State the blood parasite species.
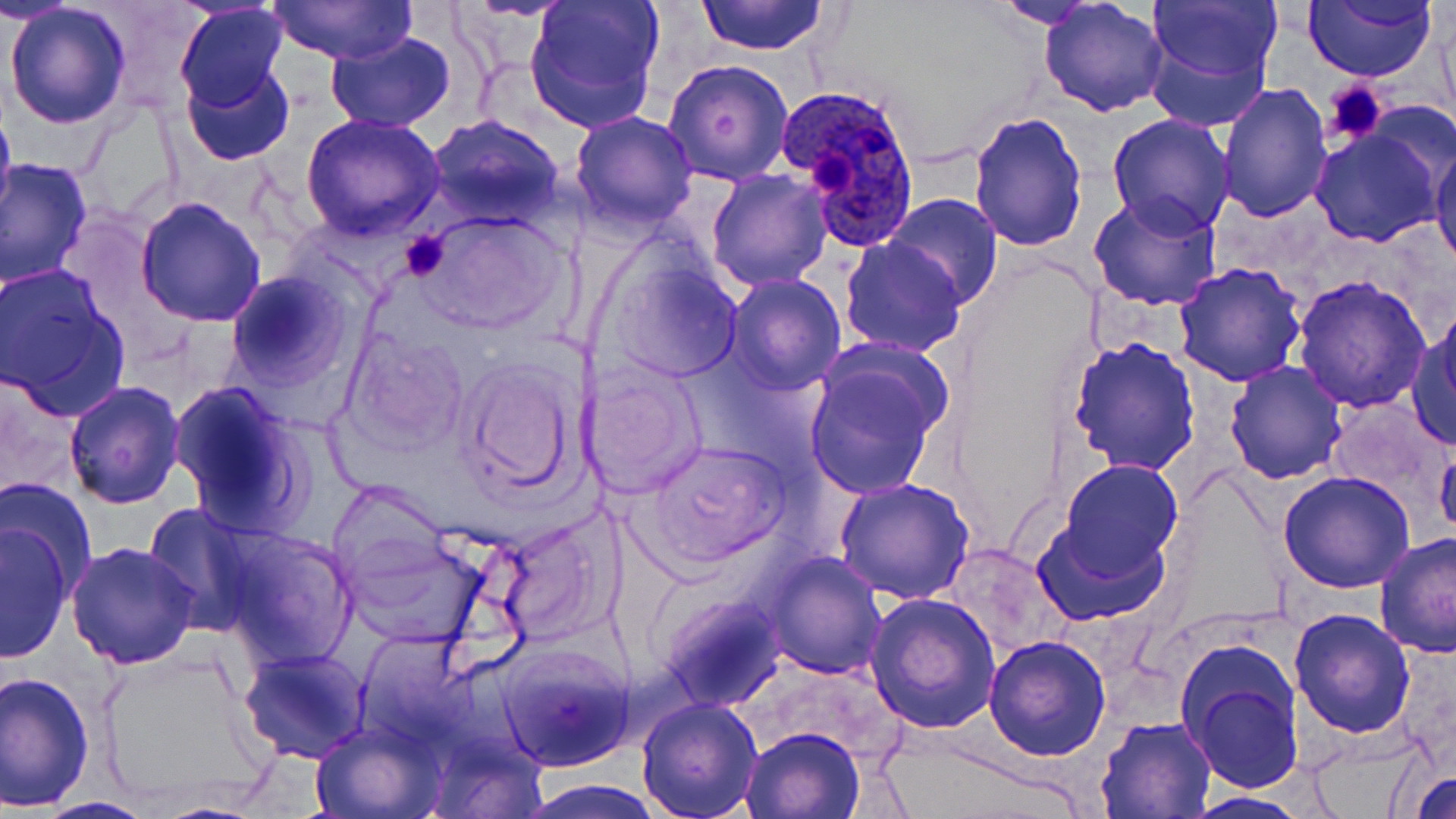
Plasmodium ovale.

Summary:
  - Coordinate format: approximate bounding boxes as (x1, y1, x2, y2) in pixels
  - Platelet locations: (1324, 79, 1387, 145), (400, 229, 453, 281)
  - Plasmodium ovale-infected red blood cell locations: (778, 84, 925, 252)
  - Uninfected red blood cell locations: (3, 0, 78, 26), (463, 0, 577, 21), (522, 0, 666, 132), (696, 0, 829, 55), (990, 0, 1109, 29), (1040, 0, 1168, 117), (1143, 0, 1280, 98), (1303, 0, 1438, 82), (269, 1, 416, 64), (5, 3, 132, 129), (174, 5, 289, 113), (324, 31, 456, 130), (663, 59, 793, 186), (182, 62, 295, 167), (1216, 82, 1333, 224), (0, 96, 16, 235), (968, 110, 1089, 252), (569, 111, 700, 232), (1106, 114, 1235, 238), (300, 115, 447, 242), (427, 116, 564, 227), (1308, 126, 1443, 247), (1430, 136, 1456, 271), (1, 157, 94, 290), (706, 170, 832, 292), (1090, 191, 1225, 313), (882, 195, 1005, 308), (135, 197, 266, 327), (414, 212, 568, 336), (839, 236, 967, 356), (597, 247, 745, 385), (1173, 262, 1308, 386), (0, 263, 130, 416), (226, 270, 351, 391), (723, 274, 846, 395), (1291, 274, 1431, 413), (1409, 320, 1456, 449), (345, 330, 471, 454), (1068, 335, 1200, 474), (804, 356, 945, 500), (459, 357, 585, 499), (1224, 360, 1348, 484), (580, 362, 707, 498), (63, 381, 185, 509), (168, 381, 313, 536), (1329, 398, 1453, 513), (642, 439, 792, 565), (1435, 439, 1456, 542), (1057, 459, 1182, 576), (1278, 471, 1417, 593), (1, 477, 98, 597), (834, 478, 975, 605), (331, 480, 448, 587), (137, 502, 265, 632), (1032, 516, 1171, 625), (491, 517, 614, 644), (0, 523, 74, 661), (217, 530, 359, 669), (1374, 531, 1455, 658), (338, 532, 493, 652), (66, 540, 200, 670), (943, 544, 1060, 657), (765, 553, 886, 679), (864, 591, 1001, 734), (660, 596, 781, 710), (1288, 608, 1417, 738), (984, 633, 1110, 760), (498, 642, 633, 772), (237, 648, 371, 765), (101, 651, 269, 810), (1179, 651, 1305, 793), (1, 669, 96, 810), (636, 697, 763, 819), (1097, 716, 1216, 817), (310, 719, 442, 818), (741, 727, 864, 818), (922, 755, 1091, 819), (1408, 768, 1456, 818), (521, 781, 663, 817), (1183, 791, 1314, 818), (36, 796, 155, 818)
  - Stain: May-Grünwald-Giemsa
  - Magnification: 1000x
  - Modality: light microscopy
  - Field of view: single
  - Image size: 1456×819 pixels
  - Preparation: thin blood smear